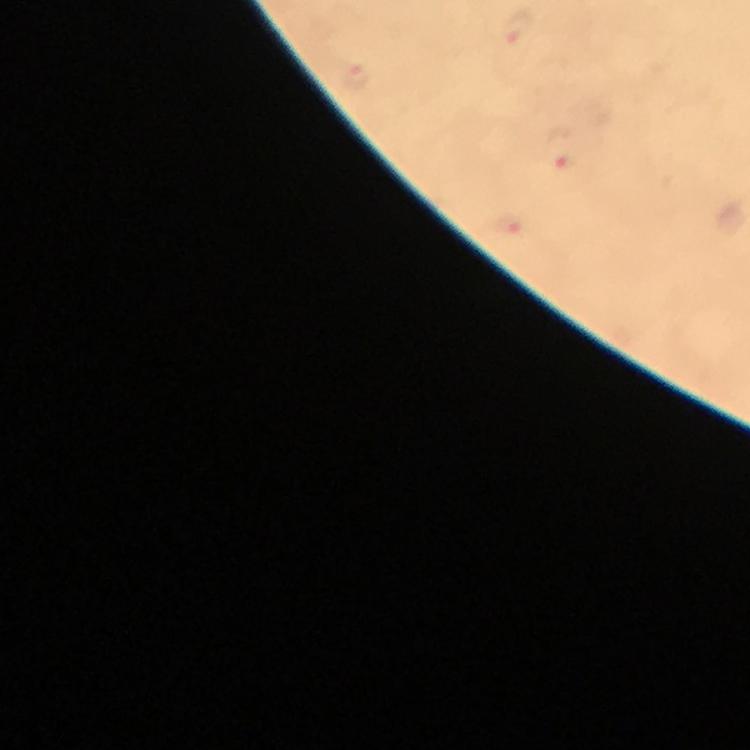
Approximate object centers, in pixels from the top-left corner.
Summary:
  - Malaria parasite locations: (x=516, y=26), (x=351, y=75), (x=560, y=156), (x=510, y=227)
  - Context: from a malaria diagnostic workup
  - Capture: smartphone camera through the microscope
  - Preparation: thick smear
  - Immersion oil: applied
  - Stain: Giemsa
  - Magnification: 100x
  - Cropped from: a single field of view
  - Image size: 750×750 pixels